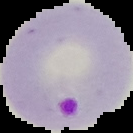 Cell region segmented out of the field of view; the surrounding area is masked to black. Image is 133×133 pixels. Malaria status: parasitized. From a thin blood film.